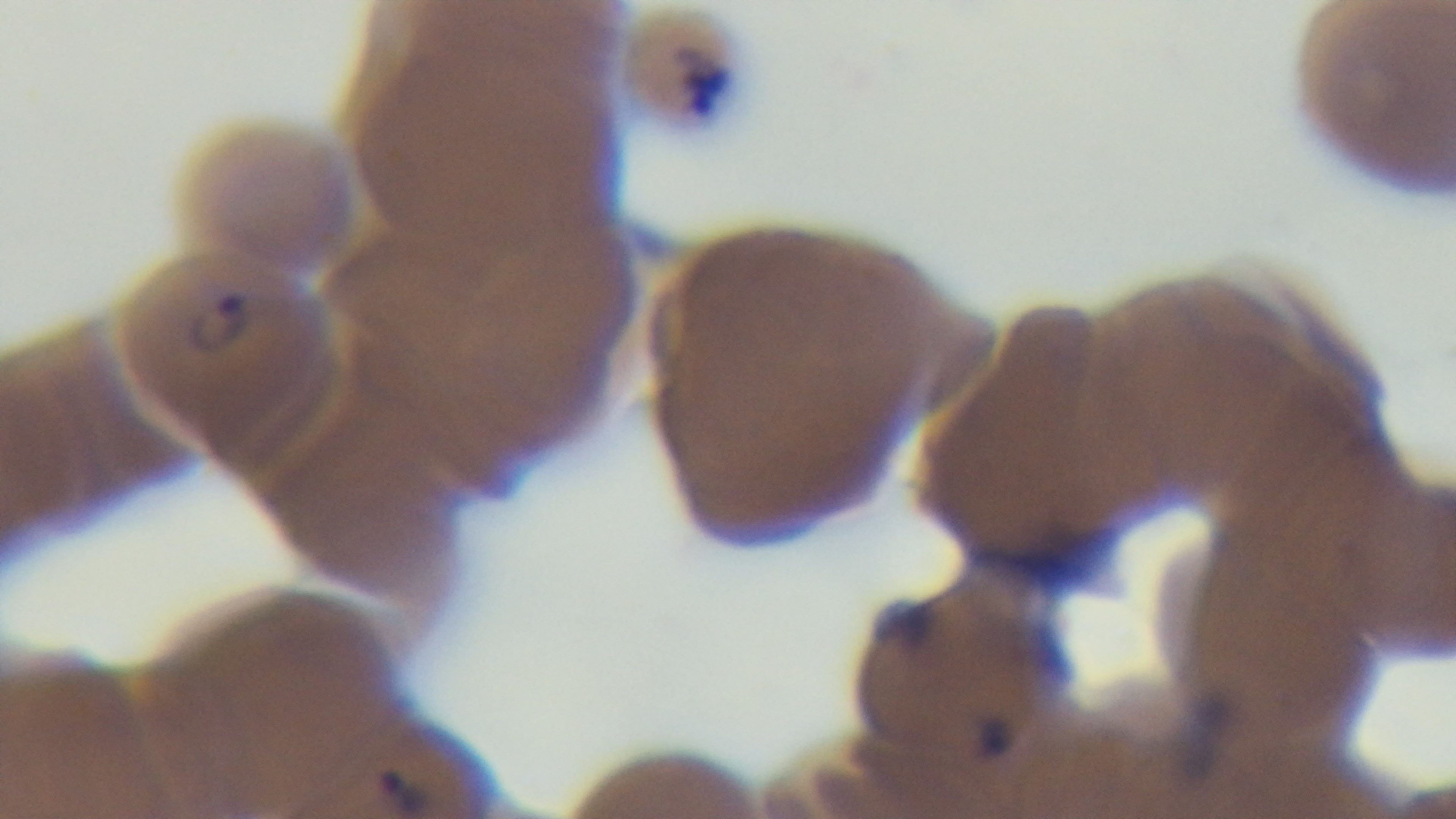
Captured with a mounted 4K digital camera. Light microscopy. Giemsa stain. Preparation: thin. Malaria status: positive. Oil-immersion objective, 100x. Single field of view.